Assess the morphology of the erythrocytes.
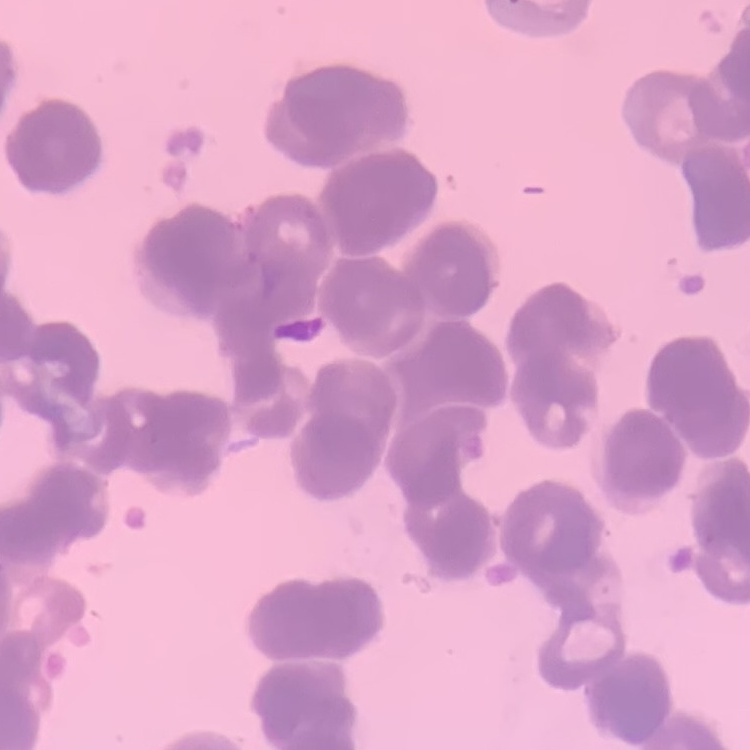

They show rouleaux formation.

One tile cut from a larger photomicrograph. Field's or Giemsa stain. Thin blood film.